Identify the preparation type.
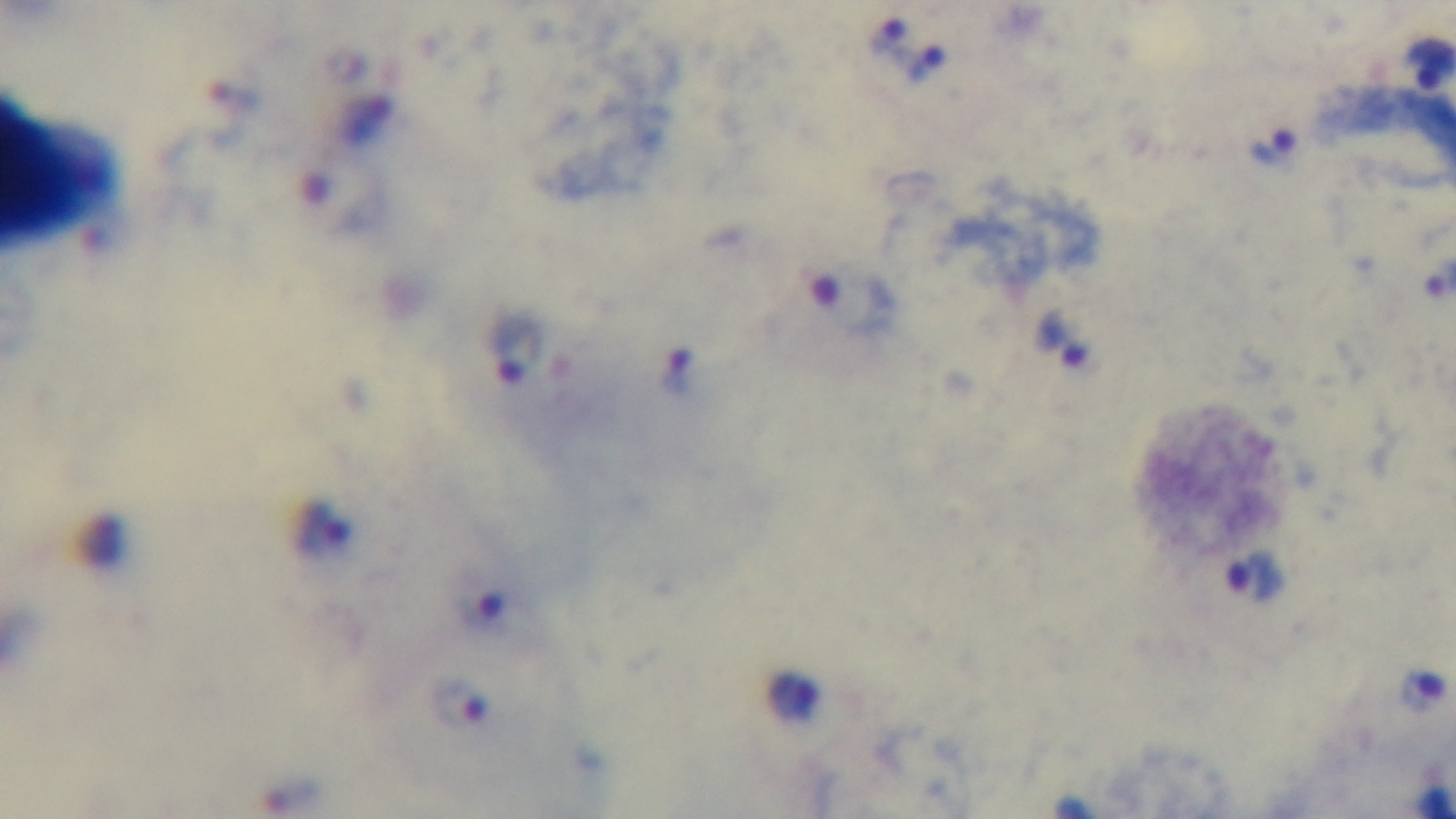
It is a thick blood film.

Summary:
  - Modality: light microscopy
  - Stain: Giemsa
  - Capture: mounted 4K digital camera
  - Objective: 100x oil immersion
  - Malaria status: positive
  - Field of view: one from the slide